Give the position of every malaria parasite.
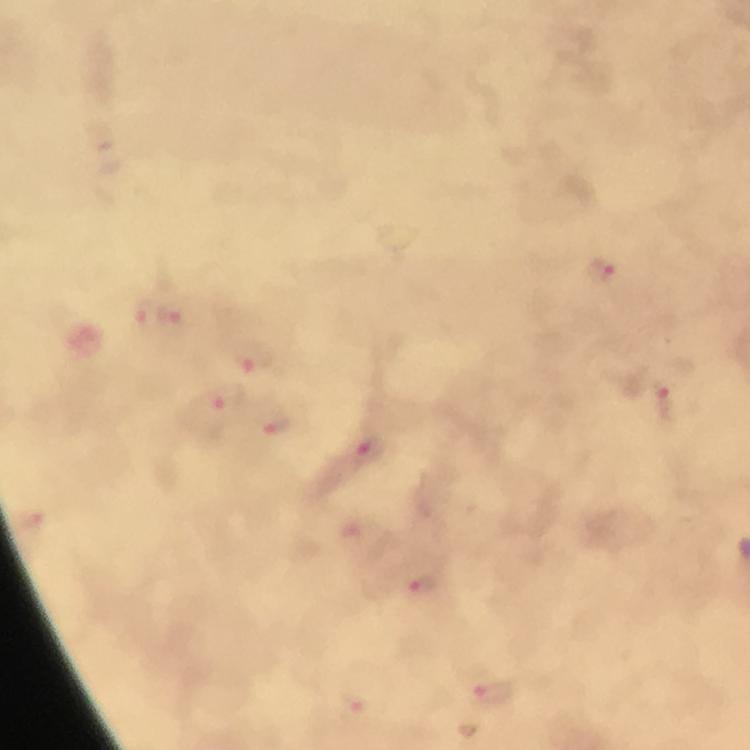

Approximate object centers, in pixels from the top-left corner.
Malaria parasites: (x=603, y=269), (x=147, y=312), (x=183, y=313), (x=258, y=362), (x=216, y=406), (x=669, y=406), (x=275, y=422), (x=366, y=447), (x=422, y=586), (x=494, y=692), (x=353, y=708).

From a malaria diagnostic workup. Immersion oil applied. Image is 750×750 pixels. A crop from one field of view. Photographed with a smartphone mounted on the microscope. Giemsa stain. Thick blood smear. 100x magnification.